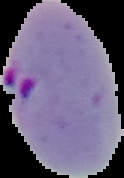
Segmented cell region on a black background. Result: malaria parasites detected. From a thin blood smear. Image is 124×178 pixels.